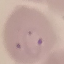
Malaria status: parasitized. Automatically extracted cell patch, resized to 64 × 64 pixels. Acquired by smartphone through the microscope eyepiece. Thin blood smear. Giemsa-stained preparation.